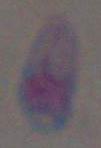

identification = Toxoplasma gondii
modality = micrograph
magnification = 1000x